Name the cell type shown.
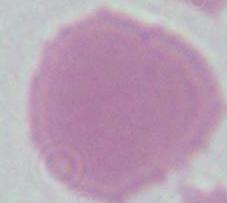
An erythrocyte.

{
  "magnification": "1000x",
  "modality": "micrograph"
}